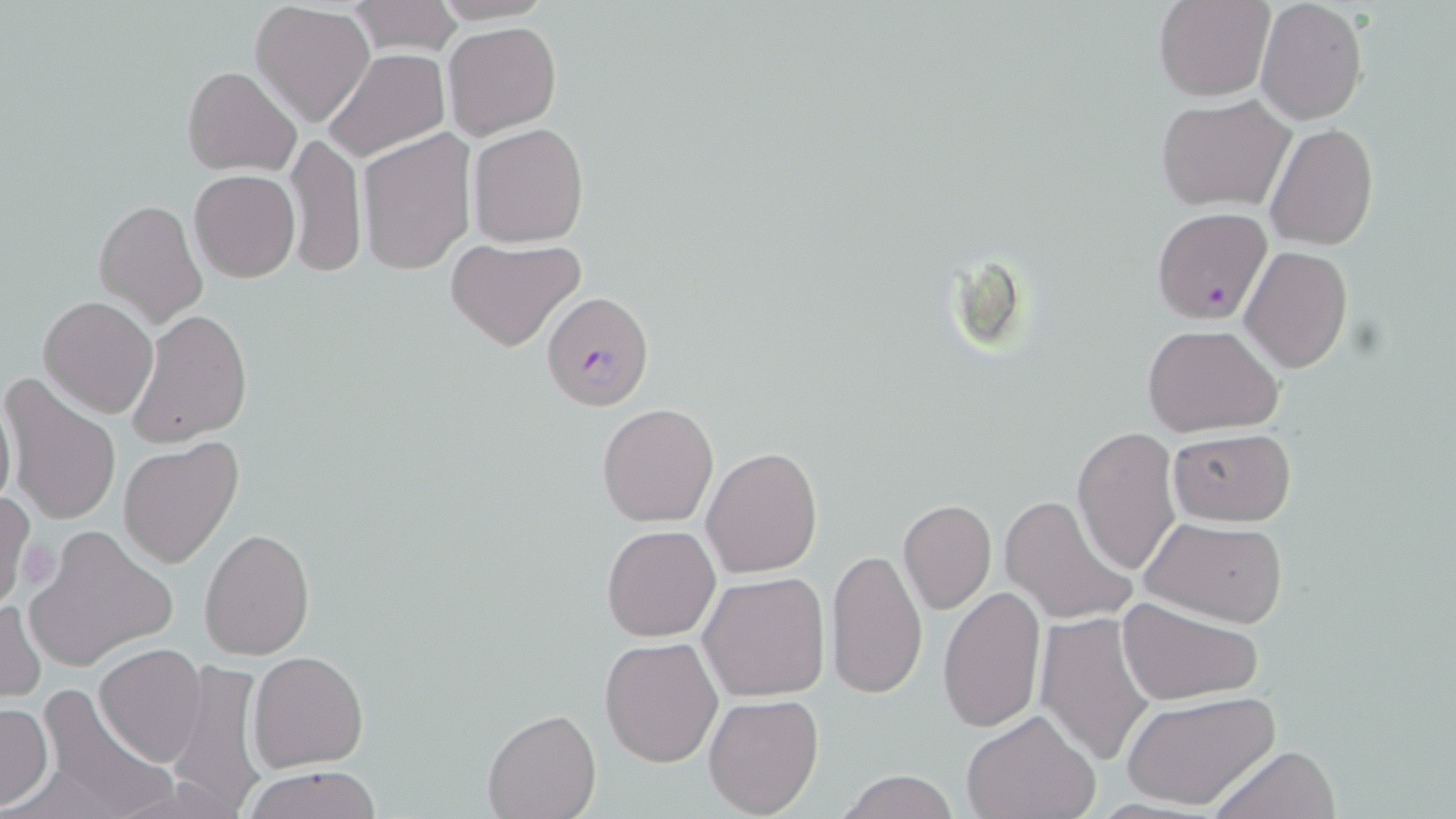

Summary:
  - Coordinate format: approximate bounding boxes as (x1, y1, x2, y2) in pixels
  - Plasmodium falciparum-infected red blood cell locations: (1150, 206, 1274, 323), (541, 291, 652, 412)
  - Platelet locations: (20, 539, 62, 594)
  - Uninfected red blood cell locations: (1154, 0, 1273, 101), (1254, 0, 1369, 125), (347, 1, 464, 56), (250, 2, 376, 127), (444, 21, 562, 139), (325, 49, 450, 161), (182, 66, 301, 176), (1156, 94, 1295, 211), (468, 123, 591, 248), (1265, 123, 1378, 250), (359, 128, 476, 274), (287, 131, 366, 278), (190, 171, 299, 281), (94, 197, 209, 329), (446, 237, 587, 352), (1240, 245, 1354, 372), (39, 295, 158, 418), (129, 311, 253, 446), (1142, 322, 1284, 437), (2, 373, 121, 526), (0, 388, 16, 516), (597, 403, 719, 527), (1071, 425, 1184, 576), (1166, 428, 1295, 526), (118, 439, 244, 568), (701, 446, 822, 579), (0, 488, 34, 614), (999, 491, 1137, 625), (898, 499, 996, 614), (1138, 514, 1290, 627), (601, 525, 721, 643), (199, 527, 315, 660), (26, 532, 174, 666), (826, 548, 928, 699), (698, 571, 830, 703), (939, 583, 1045, 733), (1, 597, 44, 705), (1117, 597, 1263, 705), (1037, 613, 1156, 767), (599, 635, 724, 768), (95, 645, 209, 767), (248, 650, 370, 773), (167, 657, 272, 811), (35, 685, 176, 818), (1120, 690, 1279, 812), (704, 694, 824, 818), (0, 704, 52, 809), (960, 708, 1100, 819), (482, 709, 600, 819), (1208, 744, 1341, 819), (243, 765, 382, 819), (837, 772, 959, 818)
  - Slide-level diagnosis: Plasmodium falciparum
  - Field of view: single
  - Preparation: thin blood smear
  - Stain: May-Grünwald-Giemsa
  - Modality: light microscopy
  - Image size: 1456×819 pixels
  - Magnification: 1000x